Point out each Plasmodium parasite.
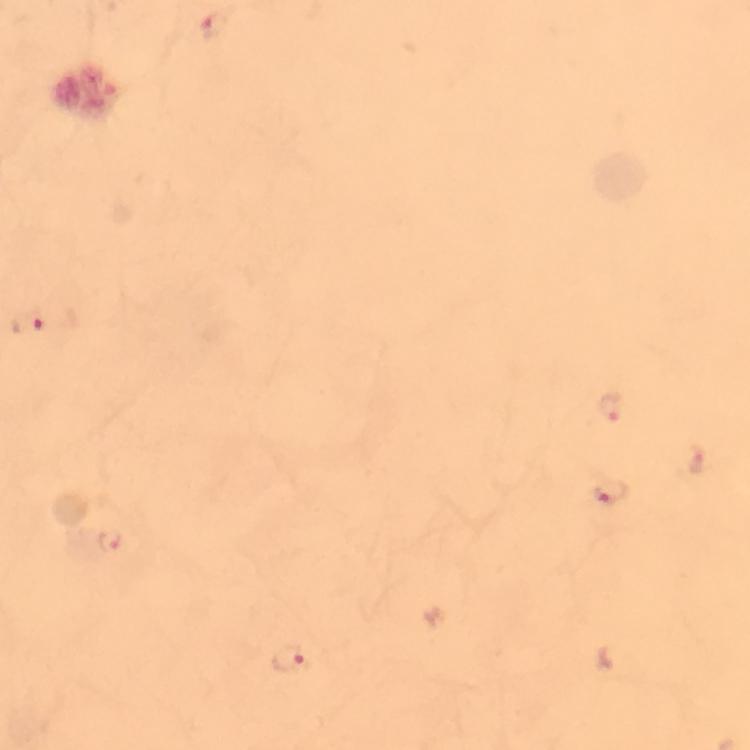
Approximate centers as {x, y} in pixels.
Plasmodium parasites: {216, 24}, {29, 322}, {611, 407}, {698, 461}, {611, 492}, {111, 541}, {289, 659}.

immersion oil = applied
image size = 750×750 pixels
cropped from = one field of view
preparation = thick blood film
capture = smartphone camera through the microscope
magnification = 100x
context = from a malaria diagnostic workup
stain = Giemsa